Classify this cell by malaria status.
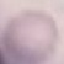
Uninfected.

Acquired by smartphone through the microscope eyepiece. Thin blood smear. Giemsa stain. Automatically extracted cell patch, resized to 64 × 64 pixels.